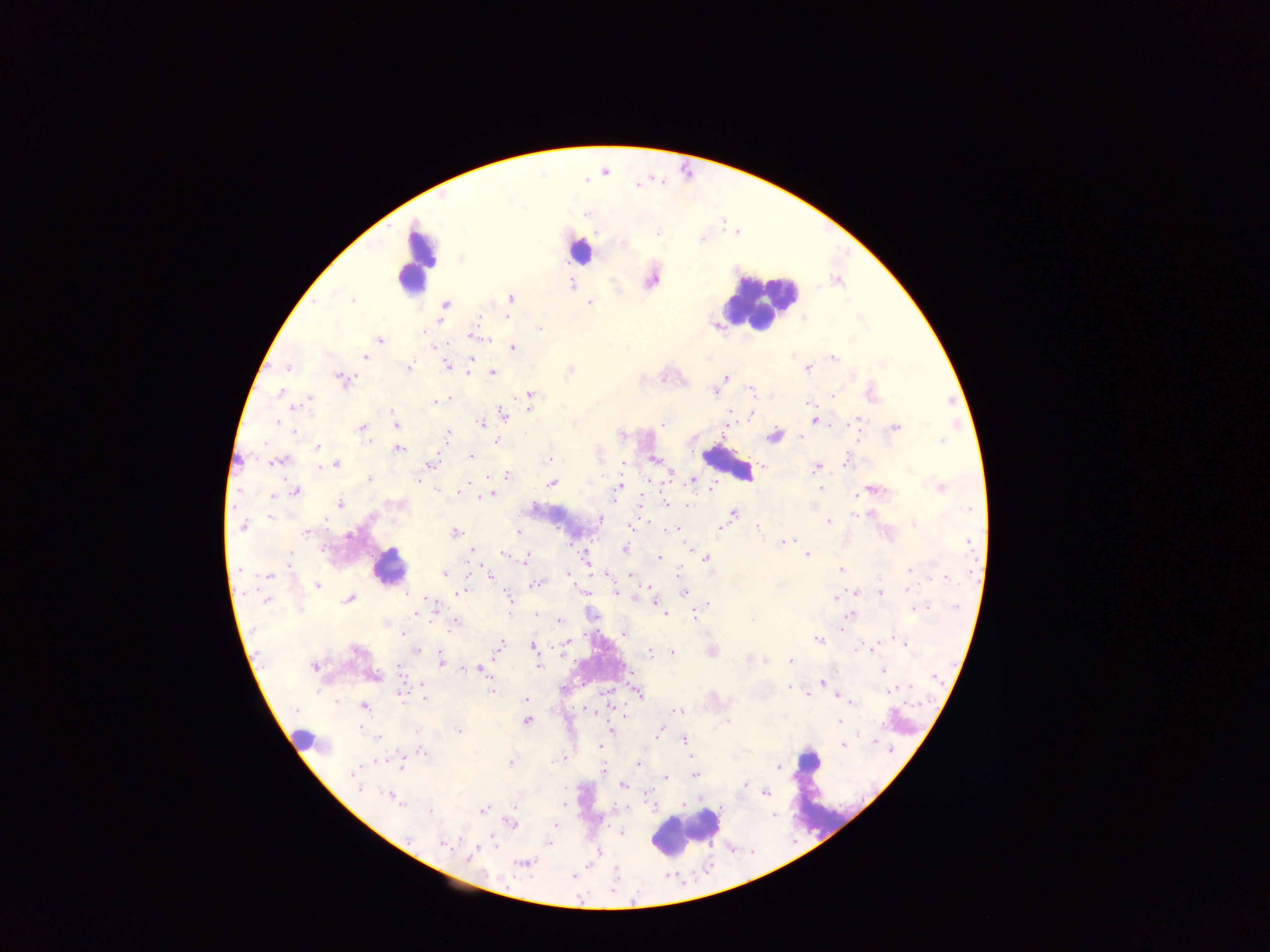
Approximate centers as x y in pixels.
Summary:
  - Plasmodium parasite locations: 596 231; 460 258; 650 277; 837 280; 510 298; 352 300; 589 302; 444 304; 507 316; 439 322; 716 326; 539 328; 472 335; 379 340; 445 345; 512 347; 365 357; 833 358; 471 359; 447 365; 807 367; 285 368; 408 368; 492 371; 726 377; 343 380; 750 389; 281 393; 715 393; 529 394; 870 394; 309 399; 450 399; 436 402; 809 402; 528 407; 729 410; 502 414; 751 415; 813 419; 663 423; 481 424; 725 424; 396 425; 362 427; 895 427; 447 433; 774 436; 494 440; 318 447; 399 448; 471 457; 549 458; 653 459; 279 460; 845 460; 335 464; 623 464; 760 464; 428 465; 817 467; 669 472; 488 477; 506 477; 369 479; 693 480; 551 482; 469 483; 619 486; 820 487; 941 487; 870 490; 295 491; 490 494; 397 503; 641 503; 665 503; 340 504; 687 504; 732 513; 599 518; 827 521; 243 526; 631 526; 757 527; 676 528; 718 528; 306 532; 455 533; 519 534; 782 542; 624 549; 689 549; 472 551; 503 553; 806 554; 585 556; 526 558; 659 558; 706 558; 841 569; 910 569; 485 572; 679 572; 445 573; 566 574; 607 574; 268 575; 490 575; 631 576; 536 583; 317 585; 584 591; 615 591; 460 592; 683 593; 879 593; 507 594; 349 598; 836 598; 266 599; 654 600; 428 601; 917 608; 434 609; 535 613; 416 614; 664 614; 693 615; 850 615; 558 621; 454 624; 841 631; 403 633; 623 633; 896 639; 501 640; 818 640; 566 641; 902 642; 500 645; 533 646; 416 650; 711 651; 648 652; 672 654; 749 657; 441 659; 765 661; 790 661; 314 666; 537 666; 465 670; 481 670; 884 670; 372 676; 821 682; 790 683; 422 686; 788 687; 492 691; 400 692; 638 693; 841 697; 425 698; 527 700; 850 701; 363 706; 587 711; 679 711; 617 712; 622 717; 525 721; 838 721; 611 730; 660 730; 683 740; 875 741; 844 744; 599 747; 420 750; 564 758; 510 763; 640 764; 401 765; 778 767; 604 771; 694 774; 665 778; 745 784; 624 785; 648 793; 765 793; 394 798; 514 807; 430 810; 483 810; 511 824; 622 832; 442 843; 549 843; 469 856; 523 863
  - Leukocyte locations: 580 250; 417 262; 761 300; 728 463; 388 566; 302 741; 808 760; 808 774; 686 829
  - Image size: 1270×952 pixels
  - Country: Ghana
  - Capture: mobile-phone photograph through a microscope
  - Field of view: single
  - Preparation: thick blood smear